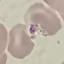
Summary:
  - Result: no malaria parasites detected
  - Stain: Giemsa
  - Preparation: thin blood smear
  - Capture: smartphone camera at the microscope eyepiece
  - Image type: automatically extracted cell patch, resized to 64 × 64 pixels